Assess this cell for malaria.
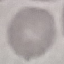
It is uninfected.

preparation: thin blood smear
capture: smartphone camera at the microscope eyepiece
stain: Giemsa
image_type: cell patch, automatically extracted from a larger field of view and resized to 64 × 64 pixels